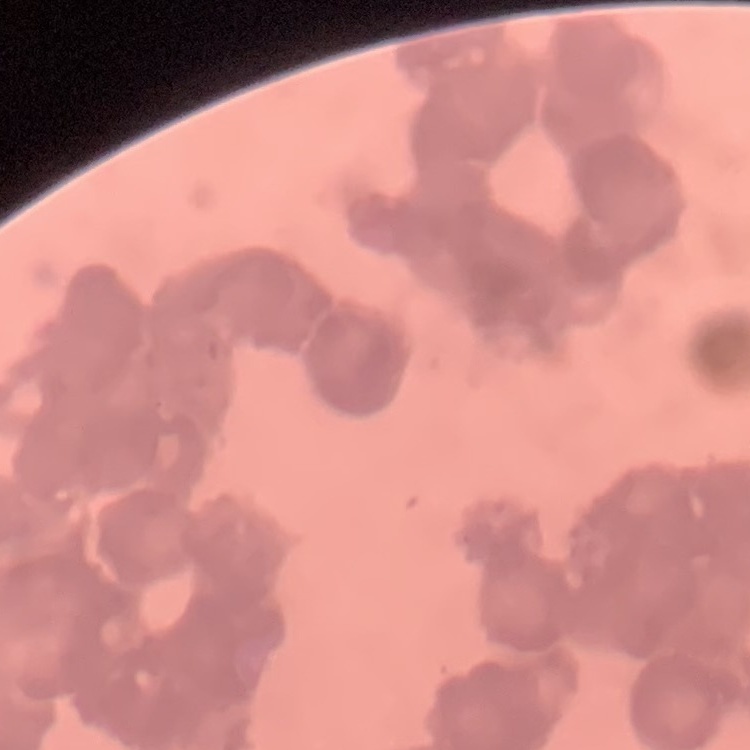

red blood cell morphology = rouleaux formation
stain = Field's or Giemsa
preparation = thin blood film
image type = square crop of a larger photomicrograph